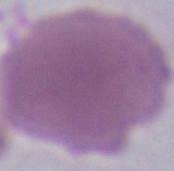

Summary:
  - Modality: photomicrograph
  - Magnification: 1000x
  - Identification: erythrocyte